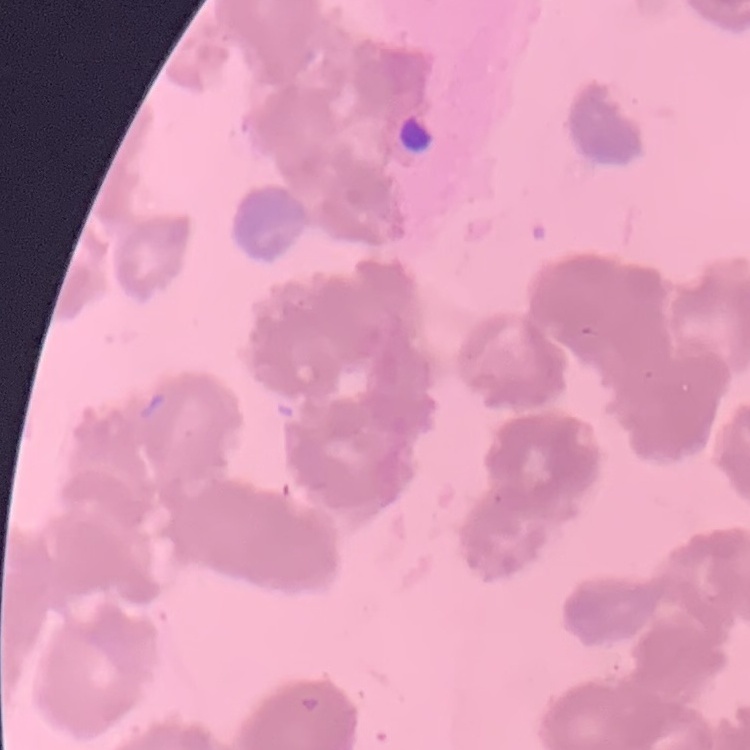

Summary:
  - Red blood cell morphology: rouleaux formation
  - Stain: Field's or Giemsa
  - Image type: square crop of a larger photomicrograph
  - Preparation: thin peripheral smear